Classify this cell by malaria status.
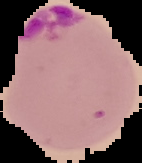

Parasitized.

image type = segmented cell region with the area outside set to black
image size = 142×163 pixels
preparation = thin blood film